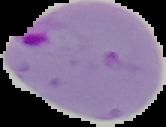 Segmented cell region on a black background. Image is 166×127 pixels. From a thin blood film. Result: Plasmodium parasites identified.